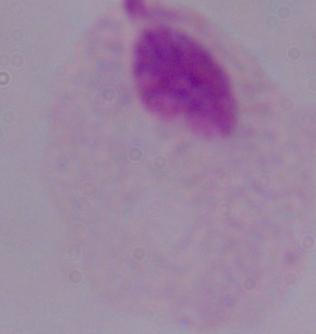

modality = micrograph
identification = trichomonad
magnification = 1000x